Give the extent of all Plasmodium vivax-infected red blood cells.
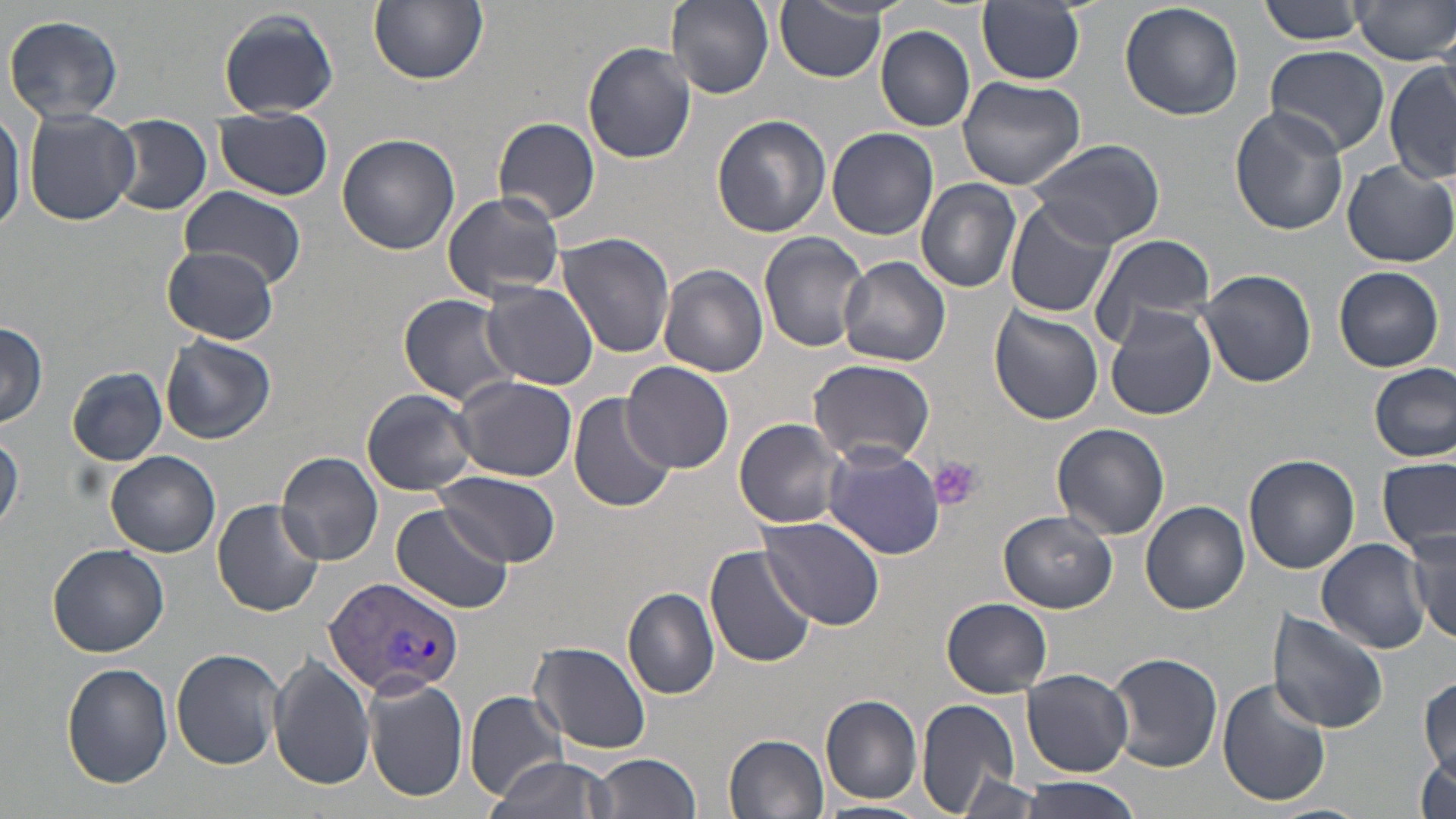

Approximate bounding boxes as (x1, y1, x2, y2) in pixels.
Plasmodium vivax-infected red blood cells: (321, 574, 467, 699).

Summary:
  - Platelet locations: (932, 456, 985, 511)
  - Uninfected red blood cell locations: (369, 0, 488, 85), (666, 0, 774, 98), (1257, 0, 1372, 46), (977, 1, 1086, 86), (1352, 1, 1456, 66), (1119, 2, 1244, 122), (776, 3, 886, 83), (218, 9, 339, 118), (4, 14, 125, 123), (875, 26, 974, 131), (583, 42, 697, 164), (1265, 45, 1390, 156), (1386, 63, 1455, 184), (956, 76, 1086, 190), (0, 104, 24, 238), (1228, 108, 1348, 236), (22, 109, 141, 226), (213, 110, 334, 200), (110, 115, 212, 216), (712, 115, 832, 239), (495, 116, 602, 225), (826, 127, 939, 239), (337, 132, 460, 256), (1022, 139, 1167, 249), (1343, 160, 1456, 267), (916, 179, 1022, 293), (180, 188, 306, 286), (441, 191, 566, 302), (1007, 198, 1120, 318), (759, 231, 871, 353), (1089, 231, 1216, 345), (556, 233, 676, 359), (158, 245, 282, 344), (840, 257, 950, 367), (660, 264, 769, 379), (1333, 266, 1444, 372), (1196, 268, 1320, 389), (479, 282, 599, 389), (399, 295, 521, 408), (989, 305, 1104, 425), (1104, 305, 1216, 420), (0, 322, 48, 429), (160, 333, 276, 444), (807, 358, 936, 466), (621, 360, 736, 472), (1370, 364, 1454, 463), (67, 366, 167, 465), (451, 375, 577, 482), (361, 389, 478, 495), (567, 393, 678, 513), (734, 418, 849, 527), (1051, 424, 1169, 541), (1, 433, 23, 535), (821, 446, 948, 561), (107, 451, 220, 557), (278, 451, 385, 567), (1245, 453, 1360, 573), (1378, 456, 1455, 555), (435, 472, 562, 568), (211, 497, 325, 615), (1140, 500, 1250, 614), (390, 501, 512, 613), (998, 509, 1117, 613), (757, 517, 882, 629), (1408, 528, 1456, 645), (1317, 539, 1429, 654), (46, 543, 169, 658), (705, 543, 818, 669), (625, 570, 803, 689), (622, 588, 720, 699), (941, 598, 1053, 697), (1266, 609, 1390, 733), (530, 641, 652, 754), (171, 649, 286, 769), (1106, 651, 1224, 773), (268, 654, 374, 791), (61, 663, 174, 789), (1022, 669, 1132, 777), (1419, 672, 1455, 779), (365, 678, 468, 805), (1216, 678, 1332, 809), (464, 690, 568, 800), (821, 693, 923, 804), (916, 698, 1023, 815), (723, 732, 828, 817), (1414, 748, 1455, 819), (589, 753, 702, 819), (486, 756, 617, 819), (955, 774, 1048, 817), (1017, 777, 1146, 819), (814, 800, 926, 819)
  - Slide-level diagnosis: Plasmodium vivax
  - Image size: 1456×819 pixels
  - Field of view: one of a larger specimen
  - Modality: light microscopy
  - Preparation: thin blood film
  - Magnification: 1000x
  - Stain: May-Grünwald-Giemsa